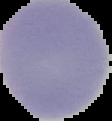 Segmented cell region on a black background. Image is 112×121 pixels. From a thin blood smear. Malaria status: uninfected.